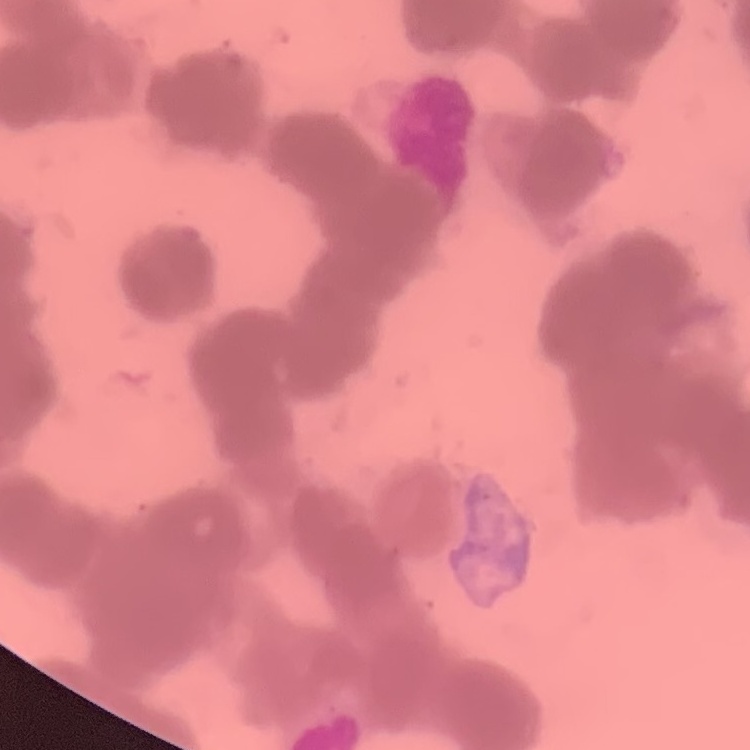

Summary:
  - Red blood cell morphology: rouleaux formation
  - Stain: Field's or Giemsa
  - Image type: one tile cut from a larger photomicrograph
  - Preparation: thin blood smear